Outline each blood parasite and name the species.
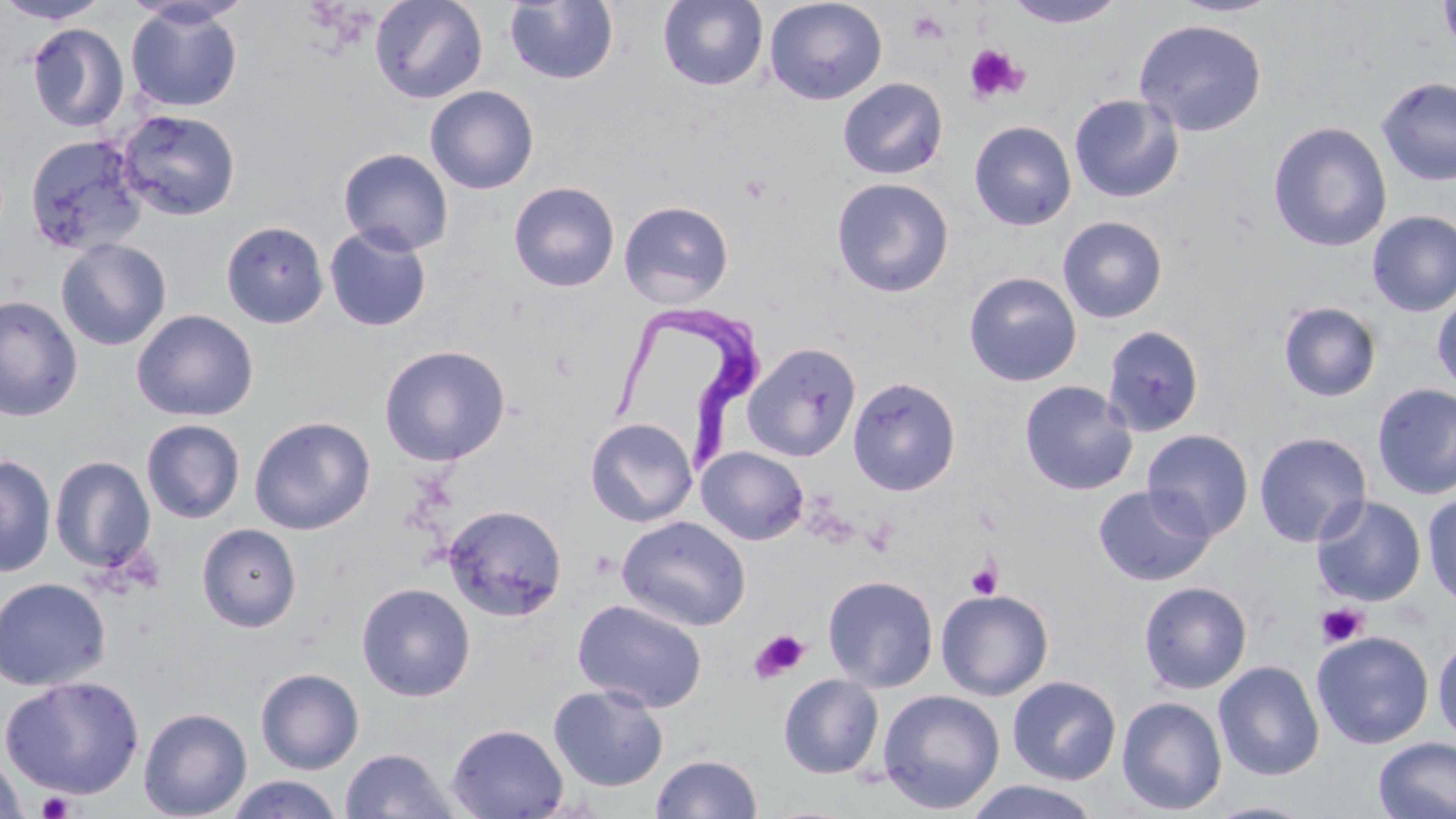

Approximate bounding boxes as (x1,y1)-(x2,y2) corner pairs in pixels.
Trypanosoma brucei: (609,303)-(763,477).
No Plasmodium falciparum, Plasmodium ovale, Plasmodium malariae, Plasmodium vivax, or Babesia divergens observed.

{
  "slide_level_diagnosis": "Trypanosoma brucei",
  "magnification": "1000x",
  "image_size": "1456×819 pixels",
  "preparation": "thin blood smear",
  "field_of_view": "single",
  "modality": "optical microscopy",
  "platelet_locations": "approximate bounding boxes as (x1,y1)-(x2,y2) corner pairs in pixels: (907,9)-(947,43), (963,43)-(1028,104), (738,172)-(771,204), (861,517)-(897,557), (966,560)-(1002,599), (1317,603)-(1369,648), (748,629)-(810,683), (36,791)-(75,818)",
  "stain": "May-Grünwald-Giemsa",
  "uninfected_red_blood_cell_locations": "approximate bounding boxes as (x1,y1)-(x2,y2) corner pairs in pixels: (0,0)-(111,24), (369,0)-(488,104), (504,0)-(619,85), (658,0)-(768,91), (763,0)-(888,105), (1002,0)-(1129,28), (1167,0)-(1284,18), (1438,1)-(1456,53), (125,2)-(244,113), (1133,18)-(1268,137), (27,23)-(129,133), (1375,76)-(1456,187), (837,77)-(948,180), (425,85)-(539,195), (1069,93)-(1184,204), (115,108)-(241,221), (969,120)-(1077,231), (1267,121)-(1393,253), (24,134)-(148,255), (338,147)-(454,256), (831,177)-(955,298), (508,181)-(619,292), (618,200)-(734,308), (1367,210)-(1456,317), (1057,216)-(1168,323), (221,220)-(328,328), (324,224)-(432,332), (56,238)-(172,351), (964,271)-(1082,387), (1431,290)-(1456,394), (0,296)-(83,422), (1278,301)-(1382,402), (132,309)-(259,422), (1102,324)-(1205,437), (742,342)-(862,462), (379,344)-(511,466), (847,376)-(961,496), (1019,380)-(1138,496), (1372,383)-(1456,501), (249,416)-(376,535), (586,418)-(698,527), (141,419)-(245,523), (1142,429)-(1254,541), (1253,431)-(1372,547), (697,447)-(809,545), (0,454)-(56,577), (50,455)-(156,573), (1092,484)-(1216,586), (1422,492)-(1456,609), (1312,495)-(1427,606), (442,504)-(567,622), (616,515)-(751,631), (197,523)-(302,632), (822,574)-(939,692), (0,576)-(111,691), (1138,581)-(1252,694), (356,582)-(475,701), (935,588)-(1054,700), (572,598)-(708,713), (1311,630)-(1434,749), (1432,636)-(1456,745), (1213,660)-(1325,781), (256,668)-(364,774), (778,673)-(884,779), (1,674)-(145,798), (1007,675)-(1121,785), (548,684)-(668,792), (877,688)-(1005,815), (1116,696)-(1227,815), (138,707)-(252,819), (446,723)-(568,818), (1373,736)-(1456,819), (340,747)-(459,818), (0,751)-(27,819), (651,753)-(763,819), (226,775)-(344,818), (962,780)-(1103,819), (1204,800)-(1321,819)"
}